Give the position of every Plasmodium parasite.
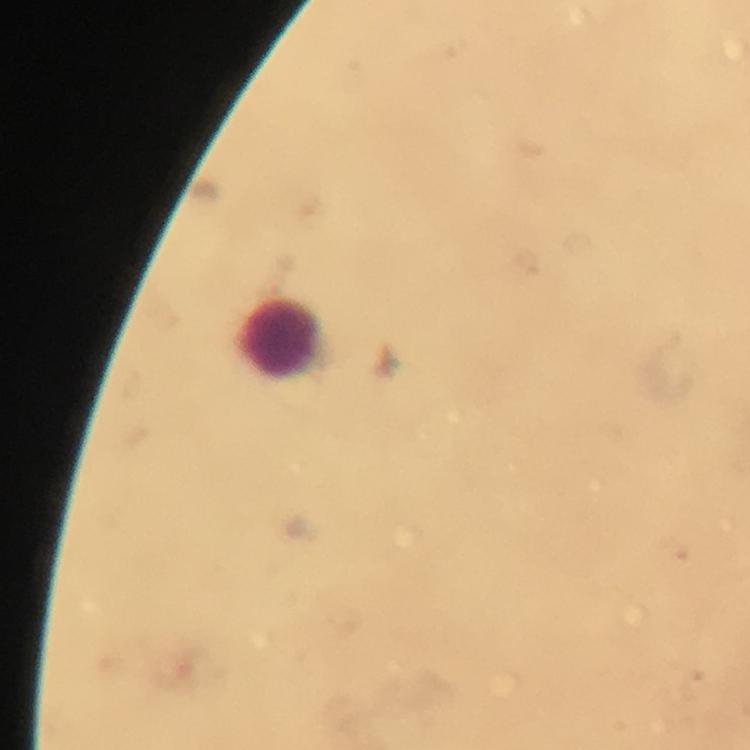

No Plasmodium parasites detected.

Approximate centers as (x, y) in pixels.
Summary:
  - Leukocyte locations: (283, 339)
  - Image size: 750×750 pixels
  - Stain: Giemsa
  - Immersion oil: used
  - Cropped from: a single field of view
  - Preparation: thick blood film
  - Context: from a malaria diagnostic workup
  - Capture: smartphone mounted on the microscope
  - Magnification: 100x